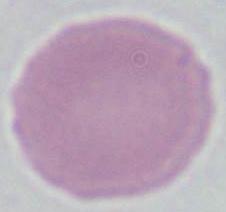

{
  "modality": "photomicrograph",
  "magnification": "1000x",
  "identification": "erythrocyte"
}